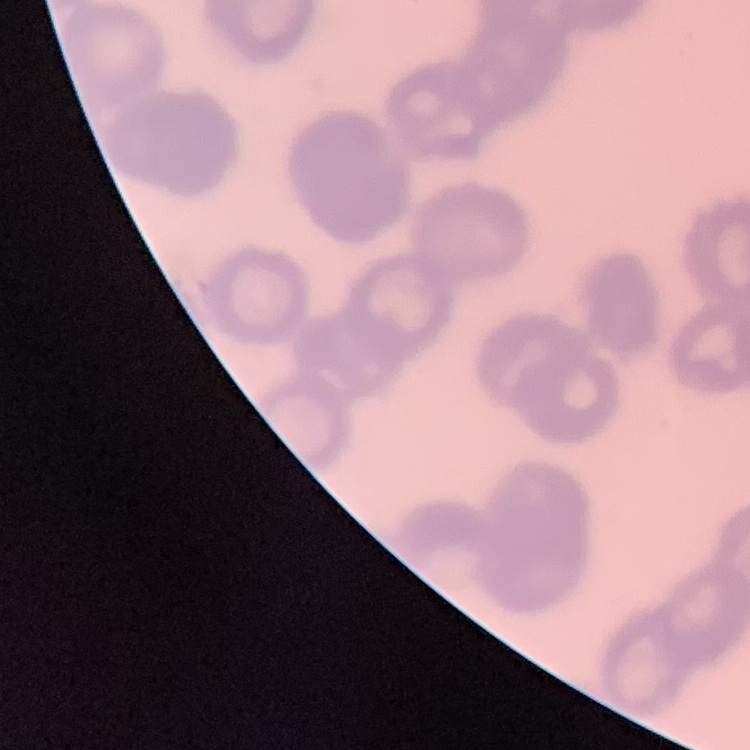
erythrocyte morphology = rouleaux formation
image type = square crop of a larger photomicrograph
stain = Field's or Giemsa
preparation = thin peripheral smear